Locate every malaria parasite.
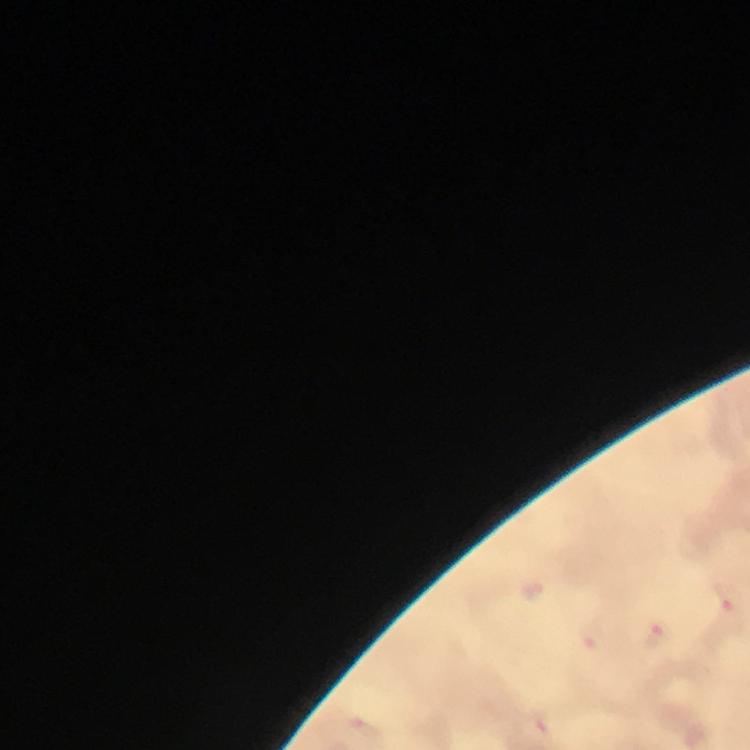

Approximate centers as (x, y) in pixels.
Malaria parasites: (660, 635).

Summary:
  - Immersion oil: applied
  - Context: from a malaria diagnostic workup
  - Image size: 750×750 pixels
  - Stain: Giemsa
  - Magnification: 100x
  - Cropped from: a single field of view
  - Preparation: thick blood smear
  - Capture: smartphone mounted on the microscope